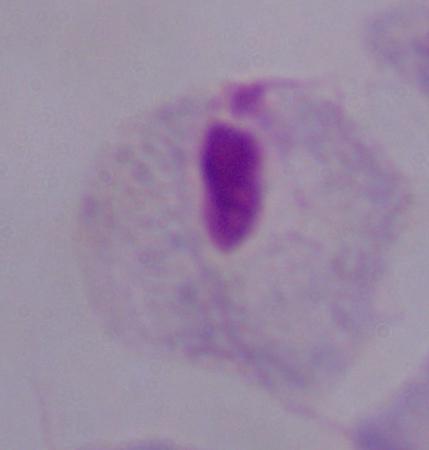
Captured at 1000x magnification. A trichomonad is shown. Photomicrograph.